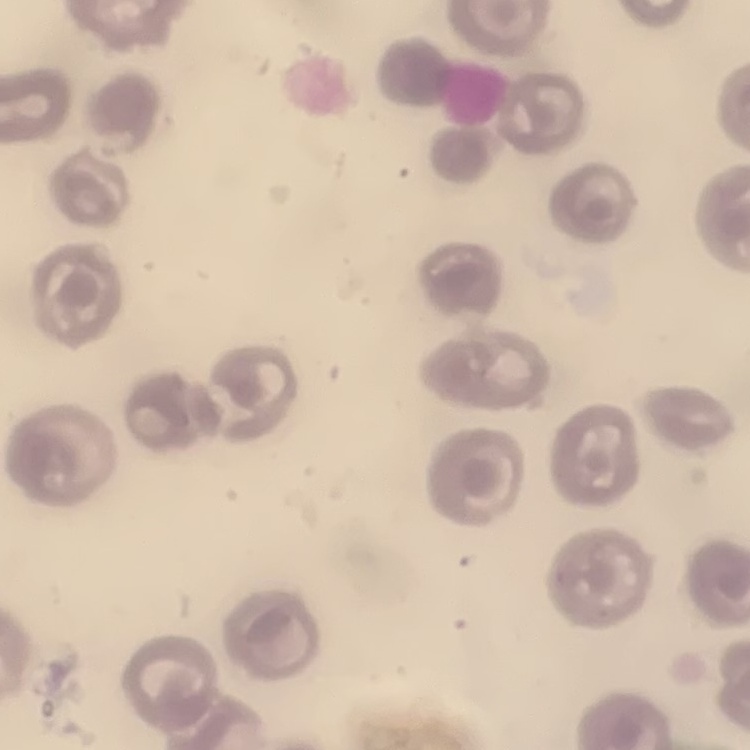

Summary:
  - Erythrocyte morphology: no rouleaux formation
  - Image type: one tile cut from a larger photomicrograph
  - Preparation: thin peripheral smear
  - Stain: Field's or Giemsa